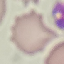
Result: negative for malaria parasites. Photographed with a smartphone camera at the microscope eyepiece. Cell patch, automatically extracted from a larger field of view and resized to 64 × 64 pixels. Thin smear of blood. Giemsa stain.